Point out each Plasmodium parasite.
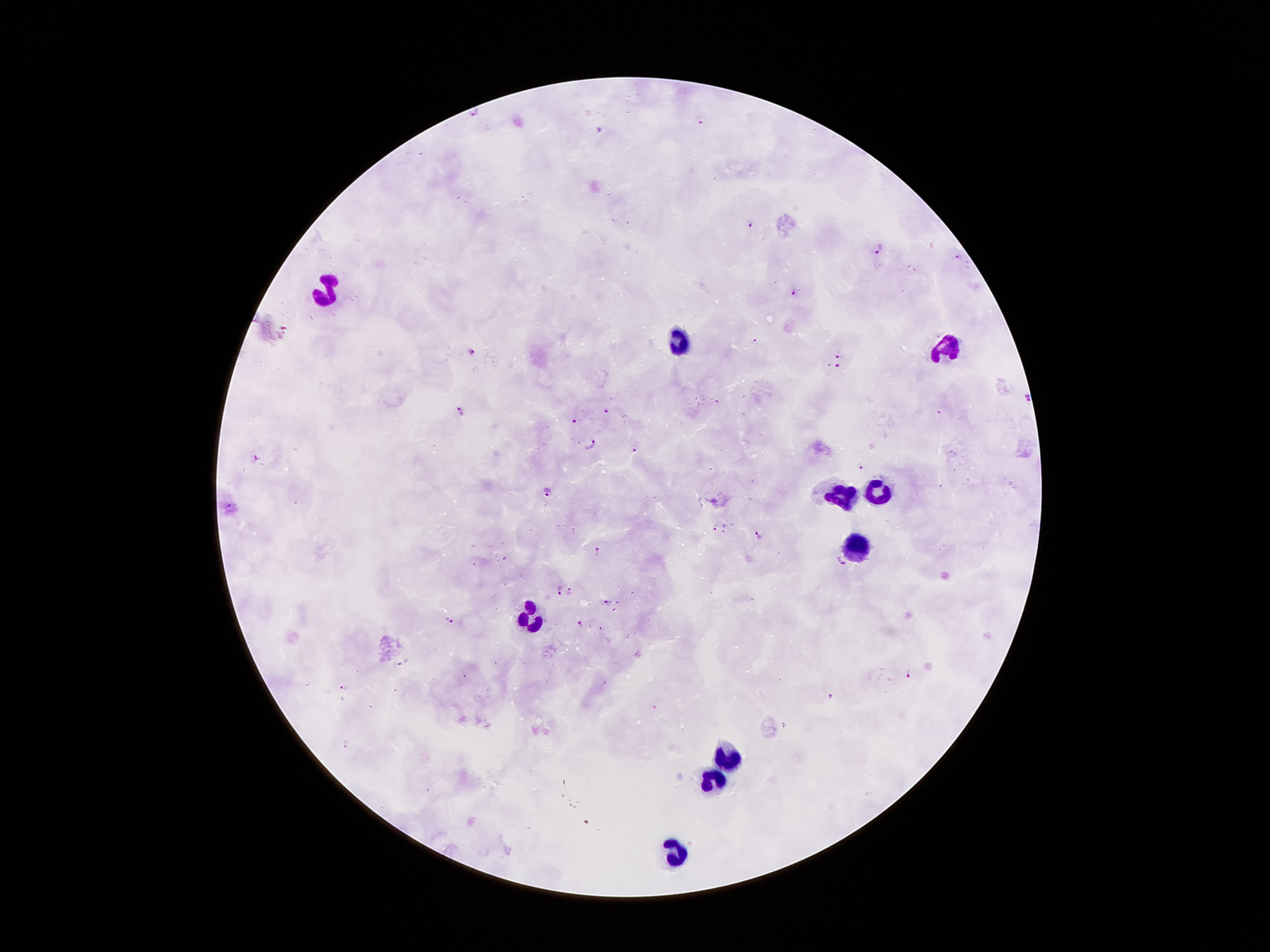
Approximate centers as (x, y) in pixels.
Plasmodium parasites: (472, 113), (700, 120), (598, 127), (751, 222), (878, 251), (957, 256), (793, 292), (756, 341), (472, 354), (840, 354), (838, 366), (1028, 397), (461, 411), (606, 412), (576, 422), (590, 444), (634, 449), (860, 466), (546, 492), (230, 506), (714, 527), (757, 536), (599, 553), (842, 563), (559, 589), (571, 590), (608, 602), (452, 621), (581, 622), (401, 663), (910, 675), (829, 696), (784, 726).

stain: Giemsa
preparation: thick blood smear
leukocyte_locations: 'approximate centers as (x, y) in pixels: (326, 291), (678, 346), (949, 346), (880, 491), (835, 496), (855, 546), (528, 616), (724, 762), (715, 782), (676, 856)'
patient_malaria_status: positive for Plasmodium falciparum
field_of_view: single
magnification: 100x
image_size: 1270×952 pixels
capture: smartphone through the microscope eyepiece